Assess this cell for malaria.
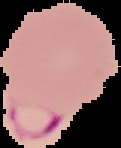

It is parasitized.

Summary:
  - Image size: 121×148 pixels
  - Preparation: thin blood smear
  - Image type: segmented cell region with the area outside set to black